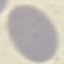

Summary:
  - Malaria status: uninfected
  - Preparation: thin blood film
  - Stain: Giemsa
  - Image type: cell patch, automatically extracted from a larger field of view and resized to 64 × 64 pixels
  - Capture: smartphone through the microscope eyepiece